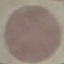
Summary:
  - Result: no malaria parasites detected
  - Image type: cell patch, automatically extracted from a larger field of view and resized to 64 × 64 pixels
  - Capture: smartphone camera at the microscope eyepiece
  - Stain: Giemsa
  - Preparation: thin blood film